Name the parasite shown.
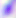
This is Toxoplasma gondii.

magnification: 400x
modality: micrograph